Assess this cell for malaria.
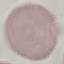
Uninfected.

Photographed with a smartphone camera at the microscope eyepiece. Thin blood smear. Giemsa-stained preparation. Cell patch, automatically extracted from a larger field of view and resized to 64 × 64 pixels.